Evaluate for parasitized red blood cells.
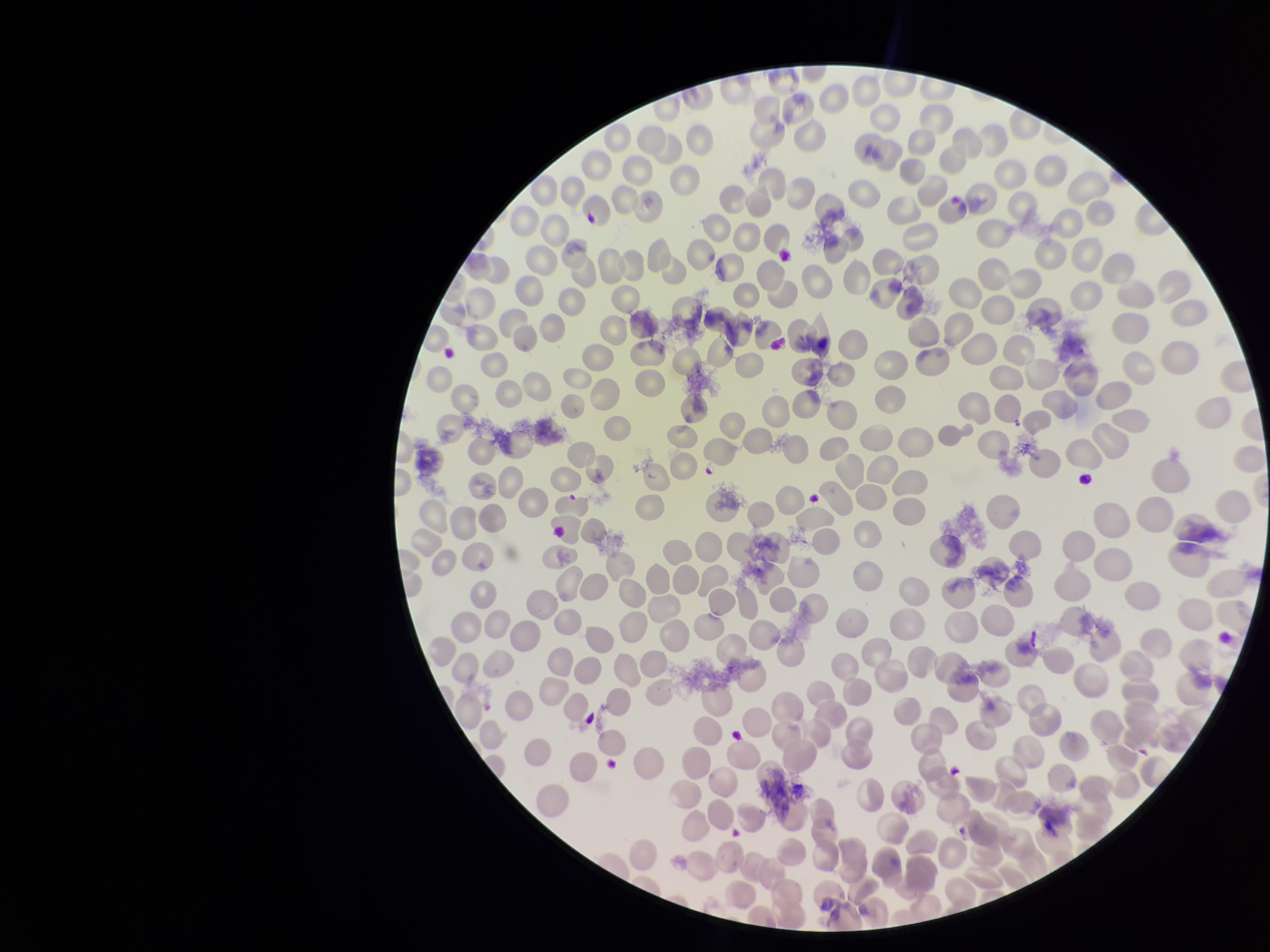
None detected.

Summary:
  - Red blood cell count: 324
  - Species reported for this patient: Plasmodium vivax
  - Field of view: one from this slide
  - Patient malaria status: positive
  - Stain: Giemsa
  - Parasitized red blood cell count: 0
  - Capture: smartphone photograph through the microscope eyepiece
  - Preparation: thin smear
  - Image size: 1270×952 pixels